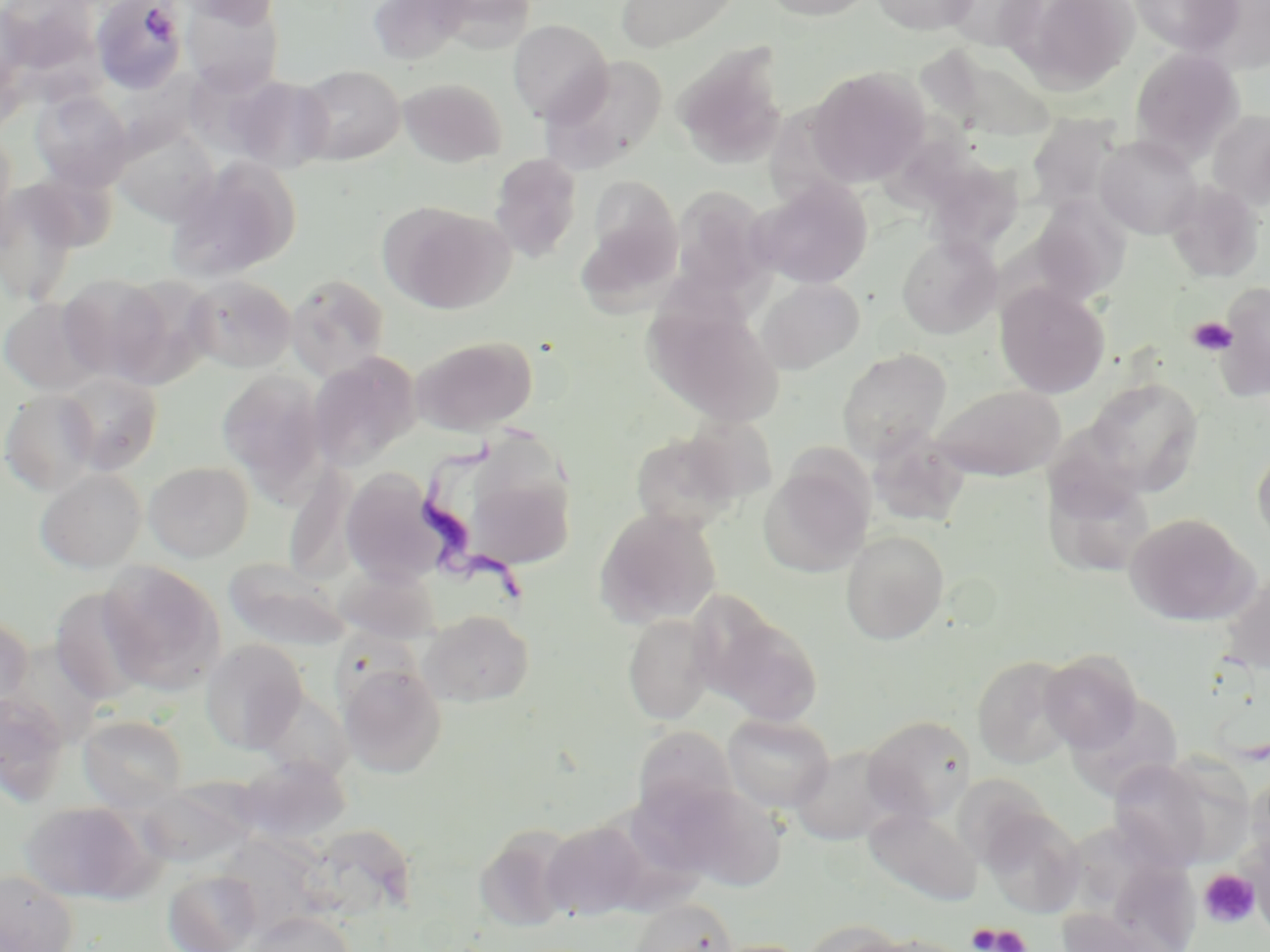
Summary:
  - Coordinate format: approximate bounding boxes as named x1/y1/x2/y2 corners in pixels
  - Trypanosoma brucei locations: (x1=418, y1=437, x2=538, y2=611)
  - Platelet locations: (x1=141, y1=5, x2=178, y2=42), (x1=1188, y1=315, x2=1237, y2=356), (x1=1198, y1=869, x2=1260, y2=928), (x1=968, y1=922, x2=1029, y2=952)
  - Uninfected red blood cell locations: (x1=3, y1=0, x2=100, y2=77), (x1=92, y1=0, x2=188, y2=94), (x1=176, y1=0, x2=281, y2=27), (x1=366, y1=0, x2=472, y2=66), (x1=428, y1=0, x2=538, y2=51), (x1=615, y1=0, x2=741, y2=53), (x1=759, y1=0, x2=880, y2=21), (x1=868, y1=0, x2=982, y2=35), (x1=939, y1=0, x2=1049, y2=52), (x1=1012, y1=0, x2=1141, y2=93), (x1=1128, y1=0, x2=1245, y2=57), (x1=181, y1=3, x2=283, y2=94), (x1=0, y1=4, x2=36, y2=99), (x1=507, y1=19, x2=612, y2=124), (x1=673, y1=42, x2=789, y2=170), (x1=1130, y1=47, x2=1244, y2=163), (x1=924, y1=51, x2=1059, y2=143), (x1=540, y1=55, x2=669, y2=175), (x1=293, y1=64, x2=405, y2=165), (x1=807, y1=67, x2=929, y2=188), (x1=223, y1=74, x2=335, y2=173), (x1=399, y1=77, x2=506, y2=167), (x1=31, y1=90, x2=133, y2=190), (x1=1207, y1=110, x2=1270, y2=211), (x1=1025, y1=113, x2=1123, y2=214), (x1=111, y1=127, x2=219, y2=227), (x1=0, y1=130, x2=20, y2=242), (x1=1095, y1=135, x2=1202, y2=239), (x1=489, y1=153, x2=582, y2=263), (x1=164, y1=157, x2=300, y2=282), (x1=18, y1=168, x2=122, y2=251), (x1=930, y1=172, x2=1030, y2=267), (x1=752, y1=179, x2=874, y2=289), (x1=1164, y1=180, x2=1265, y2=283), (x1=592, y1=181, x2=684, y2=289), (x1=0, y1=183, x2=84, y2=306), (x1=671, y1=186, x2=774, y2=298), (x1=1031, y1=195, x2=1132, y2=304), (x1=384, y1=204, x2=515, y2=315), (x1=577, y1=230, x2=676, y2=326), (x1=896, y1=234, x2=1002, y2=338), (x1=57, y1=273, x2=174, y2=383), (x1=286, y1=273, x2=391, y2=380), (x1=109, y1=274, x2=217, y2=388), (x1=183, y1=274, x2=297, y2=373), (x1=756, y1=277, x2=865, y2=374), (x1=1213, y1=282, x2=1270, y2=402), (x1=995, y1=283, x2=1110, y2=398), (x1=0, y1=296, x2=105, y2=395), (x1=647, y1=300, x2=785, y2=429), (x1=412, y1=335, x2=538, y2=434), (x1=837, y1=348, x2=952, y2=461), (x1=306, y1=353, x2=420, y2=471), (x1=217, y1=370, x2=328, y2=497), (x1=57, y1=371, x2=163, y2=474), (x1=1084, y1=376, x2=1204, y2=494), (x1=929, y1=384, x2=1065, y2=481), (x1=1, y1=389, x2=100, y2=495), (x1=678, y1=415, x2=779, y2=504), (x1=868, y1=430, x2=970, y2=528), (x1=629, y1=431, x2=743, y2=532), (x1=1252, y1=445, x2=1270, y2=550), (x1=758, y1=454, x2=875, y2=578), (x1=283, y1=460, x2=361, y2=582), (x1=143, y1=461, x2=255, y2=562), (x1=462, y1=462, x2=576, y2=571), (x1=1042, y1=467, x2=1157, y2=578), (x1=35, y1=468, x2=146, y2=573), (x1=340, y1=469, x2=448, y2=589), (x1=594, y1=507, x2=722, y2=628), (x1=1125, y1=513, x2=1254, y2=626), (x1=841, y1=530, x2=949, y2=645), (x1=225, y1=559, x2=350, y2=652), (x1=97, y1=562, x2=226, y2=694), (x1=337, y1=566, x2=442, y2=643), (x1=1219, y1=571, x2=1270, y2=677), (x1=49, y1=588, x2=153, y2=706), (x1=702, y1=606, x2=823, y2=727), (x1=418, y1=609, x2=534, y2=707), (x1=622, y1=613, x2=717, y2=725), (x1=0, y1=614, x2=33, y2=717), (x1=199, y1=639, x2=309, y2=754), (x1=1039, y1=649, x2=1143, y2=752), (x1=972, y1=654, x2=1078, y2=768), (x1=338, y1=661, x2=447, y2=778), (x1=0, y1=692, x2=71, y2=806), (x1=721, y1=713, x2=835, y2=812), (x1=77, y1=714, x2=189, y2=811), (x1=861, y1=714, x2=976, y2=823), (x1=630, y1=724, x2=740, y2=822), (x1=789, y1=744, x2=904, y2=845), (x1=1109, y1=759, x2=1216, y2=870), (x1=229, y1=762, x2=365, y2=843), (x1=1246, y1=770, x2=1270, y2=876), (x1=139, y1=775, x2=257, y2=872), (x1=658, y1=782, x2=790, y2=891), (x1=20, y1=800, x2=156, y2=903), (x1=979, y1=803, x2=1087, y2=919), (x1=863, y1=808, x2=981, y2=907), (x1=1076, y1=815, x2=1148, y2=901), (x1=542, y1=820, x2=651, y2=921), (x1=474, y1=824, x2=578, y2=933), (x1=1245, y1=833, x2=1270, y2=937), (x1=0, y1=869, x2=79, y2=952), (x1=164, y1=870, x2=262, y2=952), (x1=629, y1=897, x2=737, y2=952), (x1=1057, y1=909, x2=1178, y2=952), (x1=243, y1=911, x2=355, y2=952), (x1=800, y1=920, x2=910, y2=952), (x1=863, y1=934, x2=972, y2=952), (x1=709, y1=939, x2=813, y2=952)
  - Slide-level diagnosis: Trypanosoma brucei
  - Magnification: 1000x
  - Preparation: thin blood film
  - Stain: May-Grünwald-Giemsa
  - Image size: 1270×952 pixels
  - Modality: light microscopy
  - Field of view: single